Point out every malaria parasite.
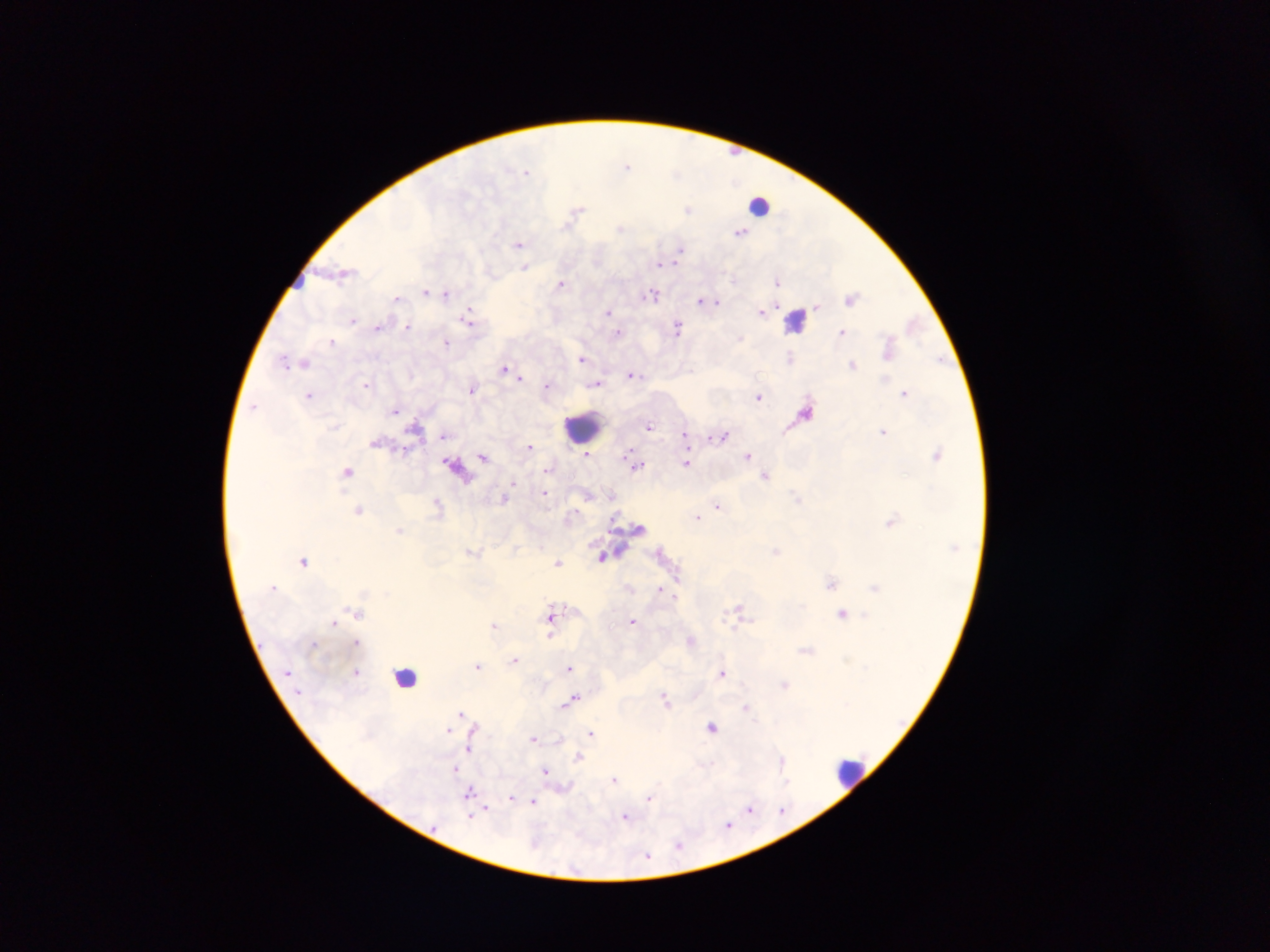
Approximate centers as (x, y) in pixels.
Malaria parasites: (627, 165), (524, 169), (528, 171), (677, 173), (688, 209), (578, 210), (568, 225), (622, 227), (740, 233), (518, 244), (680, 248), (660, 265), (677, 265), (524, 268), (733, 280), (777, 280), (561, 282), (424, 291), (433, 292), (652, 294), (447, 295), (852, 297), (397, 298), (699, 299), (717, 302), (819, 306), (607, 312), (759, 312), (469, 318), (352, 321), (379, 328), (408, 328), (677, 328), (842, 331), (616, 334), (741, 338), (332, 342), (447, 343), (887, 349), (580, 359), (790, 359), (937, 361), (289, 363), (853, 365), (502, 369), (630, 376), (520, 378), (366, 383), (548, 385), (597, 385), (472, 388), (904, 392), (310, 395), (758, 397), (254, 405), (396, 411), (647, 426), (883, 432), (686, 433), (444, 436), (725, 436), (711, 438), (528, 447), (585, 454), (483, 455), (938, 455), (749, 456), (686, 463), (639, 466), (546, 470), (348, 471), (766, 477), (512, 483), (509, 489), (546, 494), (589, 495), (505, 496), (797, 496), (437, 504), (718, 505), (358, 511), (573, 516), (698, 518), (891, 520), (401, 530), (777, 551), (305, 560), (560, 562), (831, 583), (660, 589), (677, 598), (738, 607), (844, 613), (551, 614), (336, 622), (632, 622), (495, 625), (550, 635), (692, 640), (805, 649), (516, 658), (847, 660), (478, 666), (864, 666), (568, 669), (357, 672), (722, 673), (783, 685), (576, 696), (664, 696), (572, 700), (561, 706), (746, 707), (462, 713), (712, 726), (448, 729), (592, 733), (533, 738), (560, 738), (469, 750), (580, 757), (782, 760), (456, 769), (545, 770), (614, 779), (787, 782), (468, 792), (650, 798), (511, 799), (533, 801), (488, 806), (751, 809), (783, 813), (470, 816), (626, 816), (727, 824), (678, 846), (648, 857).

Leukocyte locations: (760, 208), (796, 318), (582, 426), (405, 673), (849, 772). Mobile-phone photograph taken through the microscope. Image is 1270×952 pixels. One field of view. Sample from Ghana. Thick blood film.